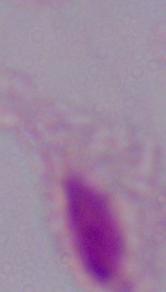

identification: trichomonad
modality: micrograph
magnification: 1000x